Give the extent of all uninfected red blood cells.
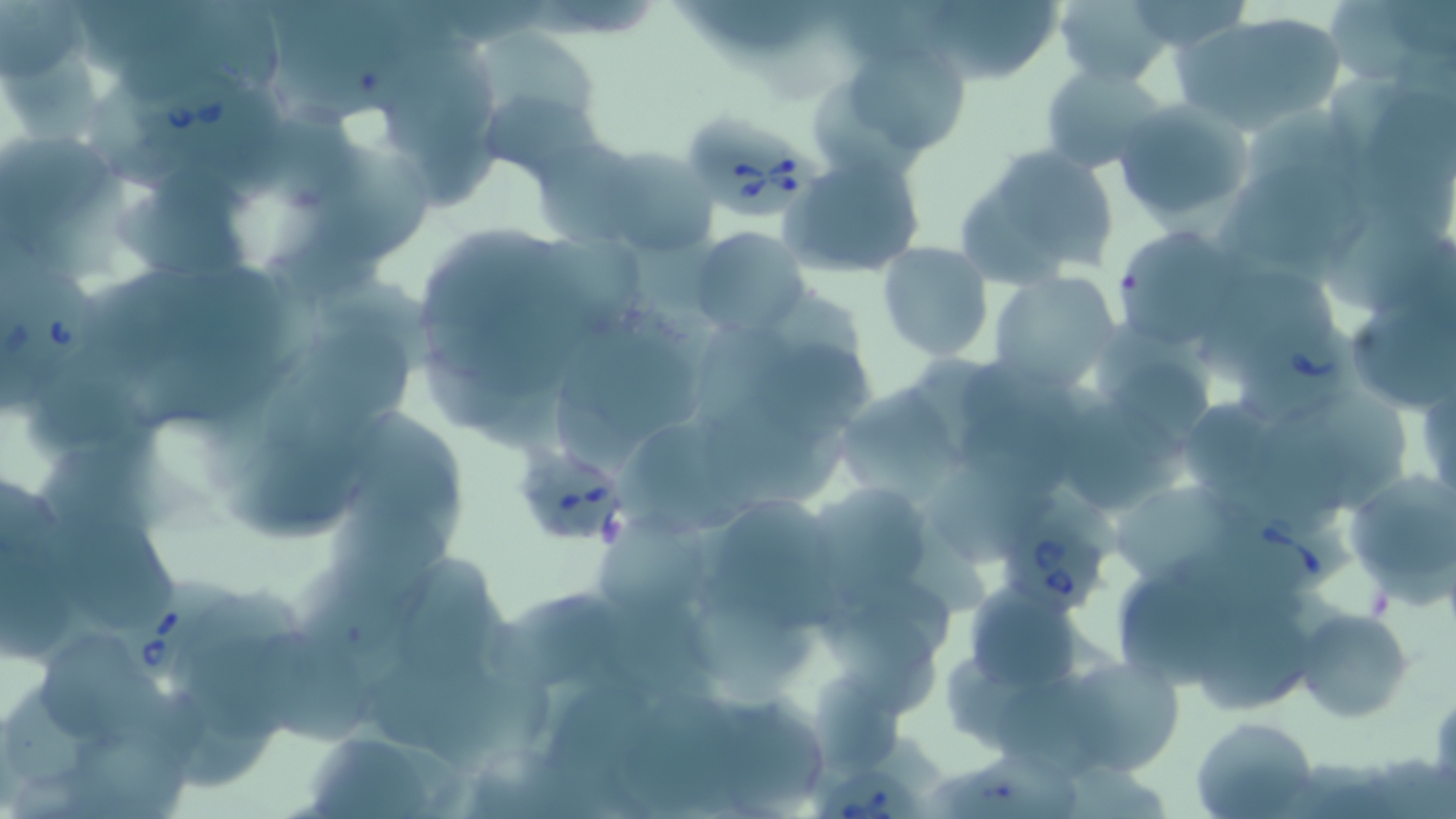
Approximate bounding boxes as (x1,y1)-(x2,y2) corner pairs in pixels.
Uninfected red blood cells: (915,0)-(1063,84), (1124,0)-(1254,54), (1324,0)-(1450,88), (1051,1)-(1175,88), (1175,14)-(1346,132), (468,26)-(601,131), (825,39)-(979,166), (1040,63)-(1172,174), (476,87)-(604,187), (1114,101)-(1254,227), (568,139)-(724,259), (954,142)-(1123,292), (305,147)-(436,264), (778,148)-(927,277), (1218,166)-(1373,269), (1108,225)-(1251,348), (690,227)-(809,337), (877,241)-(994,362), (989,269)-(1124,394), (754,334)-(871,446), (838,383)-(962,506), (1343,468)-(1455,603), (811,483)-(934,600), (54,523)-(176,627), (395,549)-(497,686), (822,604)-(941,719), (1293,607)-(1414,723), (42,634)-(168,745), (1057,658)-(1182,774), (1192,715)-(1319,819).

Summary:
  - Babesia divergens-infected red blood cell locations: (139,76)-(250,163), (686,116)-(829,219), (1,255)-(97,378), (1231,312)-(1374,425), (509,441)-(633,554), (1212,501)-(1359,597), (1002,513)-(1107,620), (112,569)-(237,692), (820,768)-(924,819)
  - Slide-level diagnosis: Babesia divergens
  - Field of view: single
  - Modality: optical microscopy
  - Stain: May-Grünwald-Giemsa
  - Image size: 1456×819 pixels
  - Preparation: thin blood film
  - Magnification: 1000x